Assess the morphology of the red blood cells.
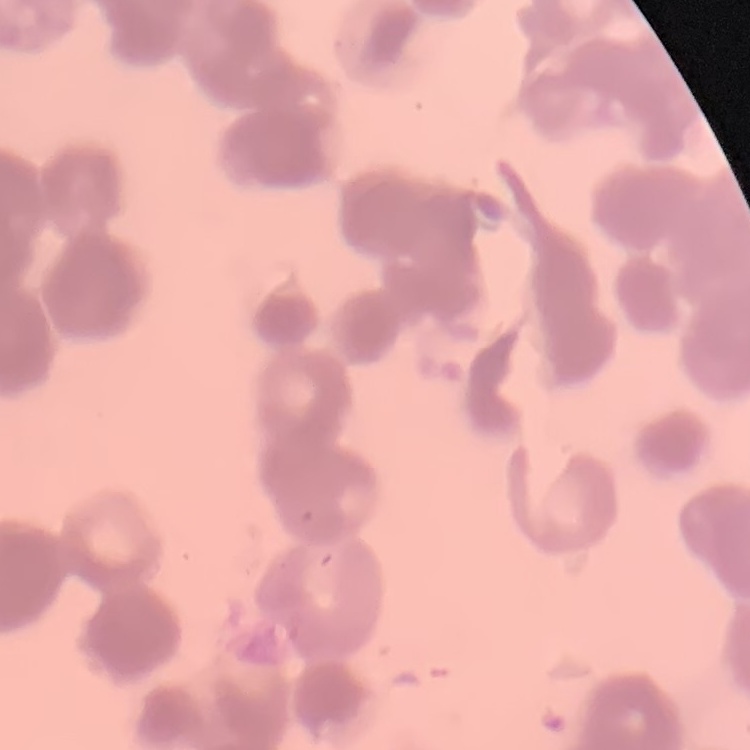
Rouleaux formation.

{
  "preparation": "thin peripheral smear",
  "stain": "Field's or Giemsa",
  "image_type": "square crop of a larger photomicrograph"
}